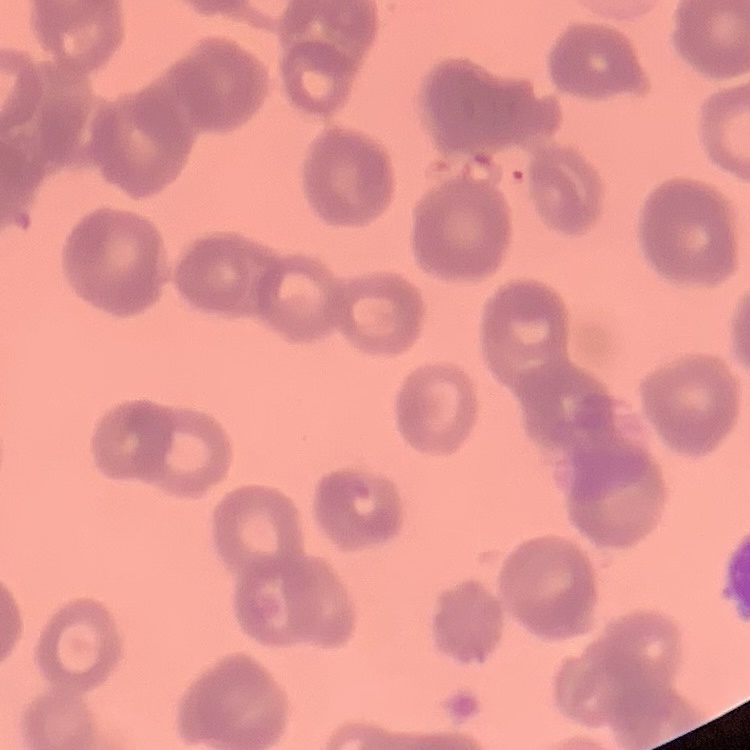

The erythrocytes exhibit rouleaux formation. Thin blood film. One tile cut from a larger photomicrograph. Field's or Giemsa stain.